Report the malaria status of this cell.
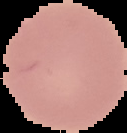
Uninfected.

From a thin blood film. Image is 127×133 pixels. Cell region segmented out of the field of view; the surrounding area is masked to black.